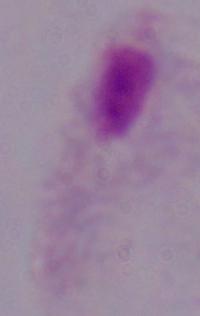

Summary:
  - Magnification: 1000x
  - Modality: micrograph
  - Identification: trichomonad